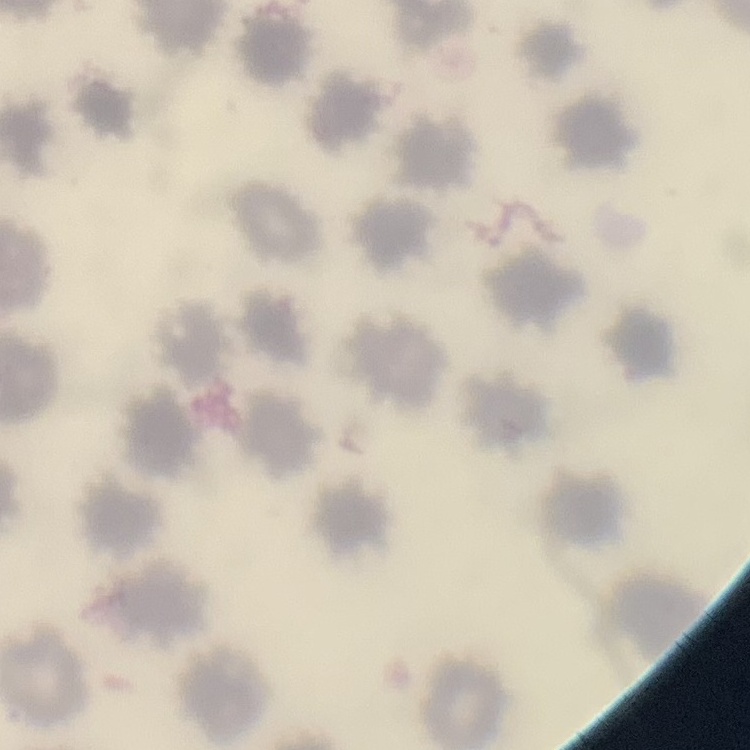

Summary:
  - Red blood cell morphology: no rouleaux formation
  - Preparation: thin blood film
  - Image type: one tile cut from a larger photomicrograph
  - Stain: Field's or Giemsa